Report the malaria status of this cell.
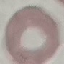

Uninfected.

Giemsa-stained preparation. Photographed with a smartphone camera at the microscope eyepiece. Cell patch, automatically extracted from a larger field of view and resized to 64 × 64 pixels. Thin blood smear.